Comment on the morphology of the erythrocytes.
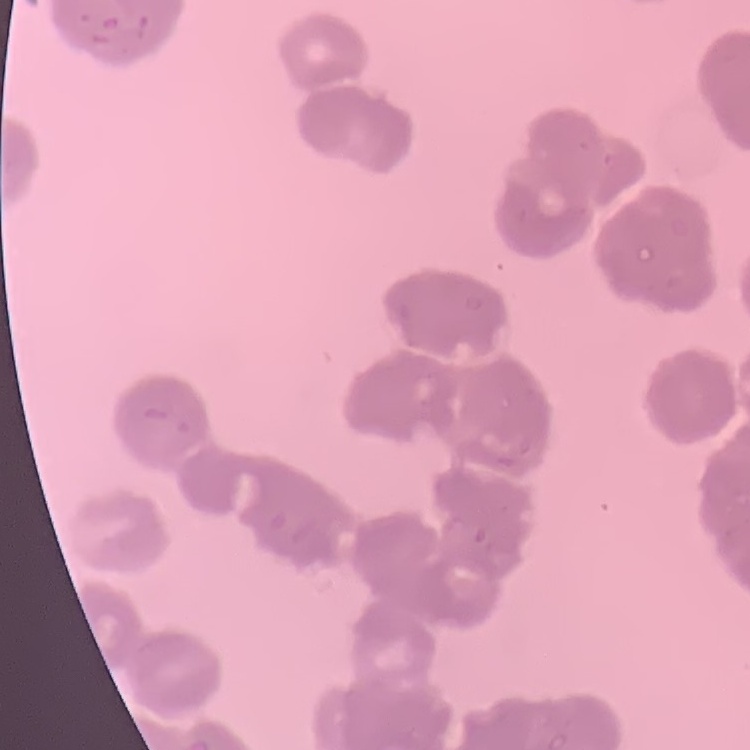

Rouleaux formation.

Thin blood smear. Field's or Giemsa stain. Square crop of a larger photomicrograph.